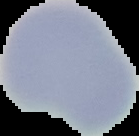

{
  "image_size": "139×136 pixels",
  "preparation": "thin blood film",
  "image_type": "segmented cell region on a black background",
  "malaria_status": "uninfected"
}